Give the position of every Plasmodium parasite and every leukocyte.
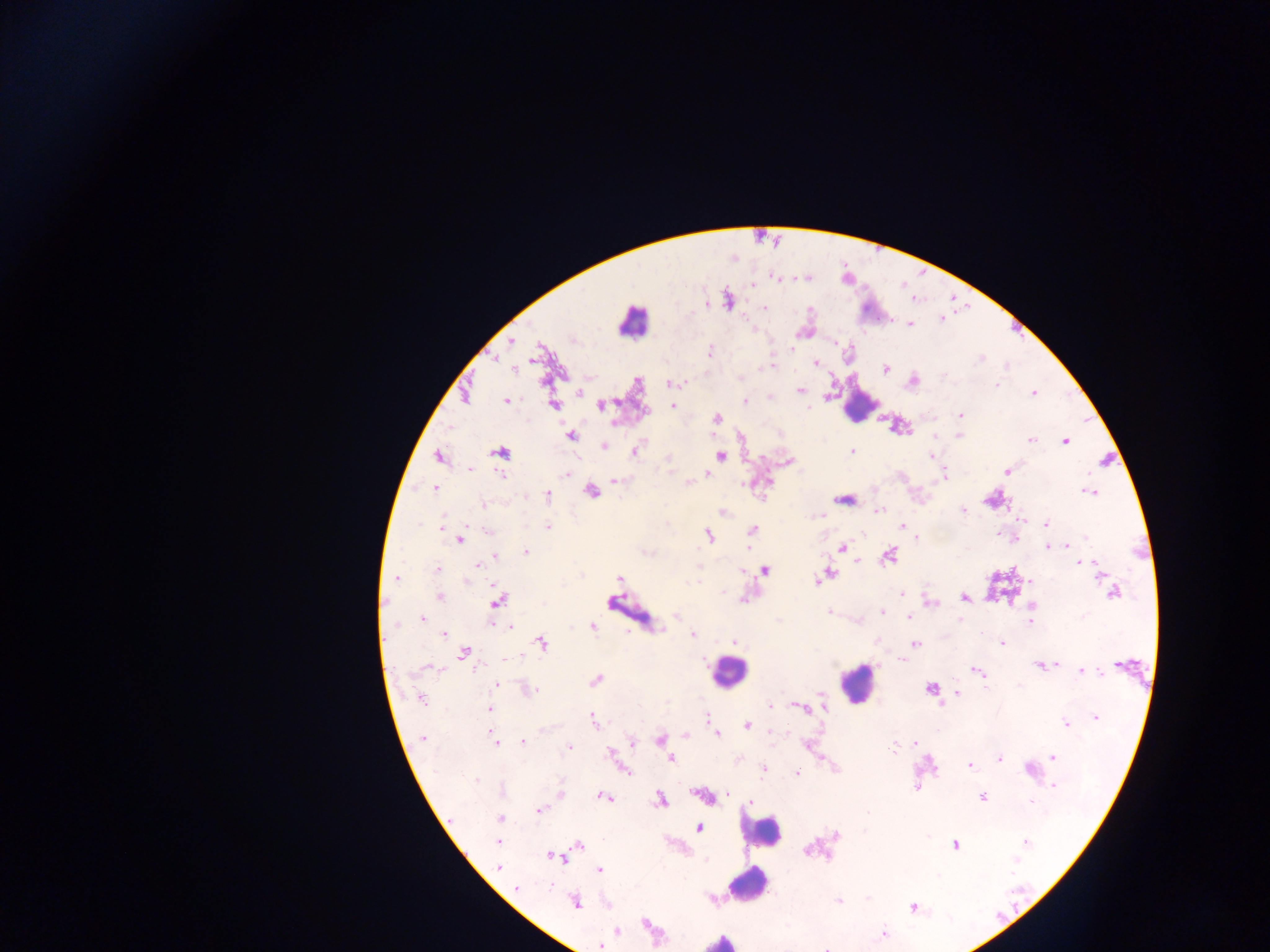
Approximate centers as (x, y) in pixels.
Plasmodium parasites: (753, 285), (706, 305), (765, 307), (941, 318), (910, 324), (510, 341), (836, 344), (711, 351), (981, 358), (816, 364), (771, 366), (514, 368), (885, 368), (913, 380), (674, 382), (997, 385), (800, 390), (579, 392), (1033, 393), (770, 398), (506, 400), (745, 401), (553, 405), (601, 405), (672, 406), (807, 407), (961, 415), (717, 419), (571, 435), (959, 436), (935, 437), (1031, 440), (1065, 441), (604, 446), (636, 451), (852, 451), (501, 453), (931, 455), (720, 456), (440, 458), (789, 461), (469, 469), (1007, 471), (565, 474), (708, 474), (502, 475), (945, 476), (616, 480), (688, 483), (435, 488), (591, 492), (1090, 492), (548, 496), (843, 500), (484, 504), (879, 511), (963, 511), (724, 512), (821, 515), (1020, 520), (419, 524), (1046, 524), (442, 526), (902, 526), (548, 527), (752, 530), (487, 531), (709, 535), (917, 537), (1086, 537), (461, 539), (1069, 545), (1047, 547), (843, 548), (526, 551), (495, 556), (889, 556), (858, 561), (1081, 563), (1087, 564), (479, 565), (1095, 566), (437, 570), (764, 571), (825, 576), (396, 578), (619, 579), (465, 581), (699, 581), (1030, 581), (901, 593), (1113, 593), (440, 595), (964, 597), (498, 600), (931, 603), (1031, 606), (829, 611), (882, 611), (677, 616), (909, 617), (422, 619), (959, 620), (1030, 621), (509, 627), (592, 627), (443, 634), (693, 634), (735, 641), (542, 643), (1002, 643), (916, 644), (464, 653), (505, 659), (904, 660), (1040, 665), (1052, 665), (430, 667), (975, 670), (1083, 671), (980, 673), (596, 680), (496, 685), (984, 686), (930, 689), (529, 690), (958, 693), (422, 699), (823, 700), (824, 705), (770, 706), (800, 707), (490, 709), (1095, 717), (707, 718), (593, 721), (1066, 724), (747, 725), (543, 730), (717, 733), (773, 733), (686, 736), (423, 738), (659, 739), (495, 742), (523, 742), (632, 742), (807, 744), (915, 744), (894, 747), (569, 748), (611, 752), (1053, 757), (671, 759), (999, 759), (970, 766), (1029, 770), (625, 771), (763, 771), (797, 773), (476, 779), (1054, 786), (915, 788), (561, 793), (727, 795), (603, 796), (704, 796), (982, 797), (660, 799), (751, 802), (1032, 802), (539, 810), (500, 818), (699, 828), (837, 835), (498, 842), (1026, 842), (955, 845), (579, 846), (807, 850), (555, 857), (1016, 861), (500, 866), (599, 870), (938, 875), (517, 888), (867, 899), (838, 901), (574, 902), (913, 908), (645, 924), (618, 930), (884, 934), (601, 946), (826, 948).
Leukocytes: (632, 321), (858, 406), (729, 672), (858, 683), (761, 831), (748, 885), (720, 941).

{
  "country": "Ghana",
  "image_size": "1270×952 pixels",
  "preparation": "thick blood smear",
  "capture": "mobile-phone photograph through a microscope",
  "field_of_view": "single"
}